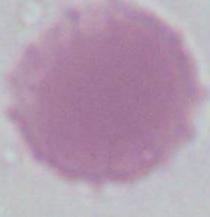

Captured at 1000x magnification. An erythrocyte is shown. Photomicrograph.